Locate Plasmodium parasites and leukocytes.
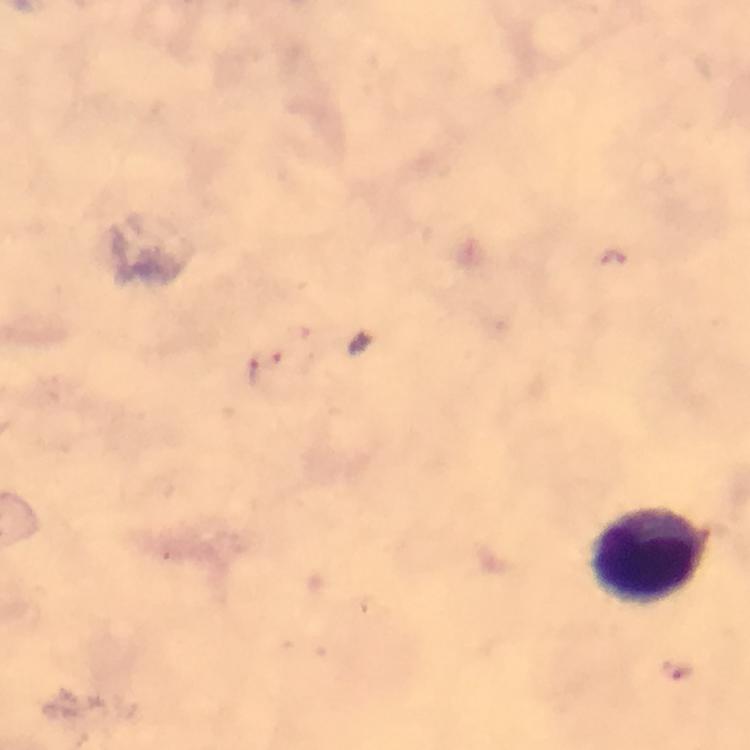
No Plasmodium parasites seen.
Approximate object centers, in pixels from the top-left corner.
Leukocytes: (x=653, y=554).

Summary:
  - Capture: smartphone mounted on the microscope
  - Context: from a malaria diagnostic workup
  - Magnification: 100x
  - Preparation: thick blood film
  - Cropped from: one field of view
  - Image size: 750×750 pixels
  - Immersion oil: used
  - Stain: Giemsa